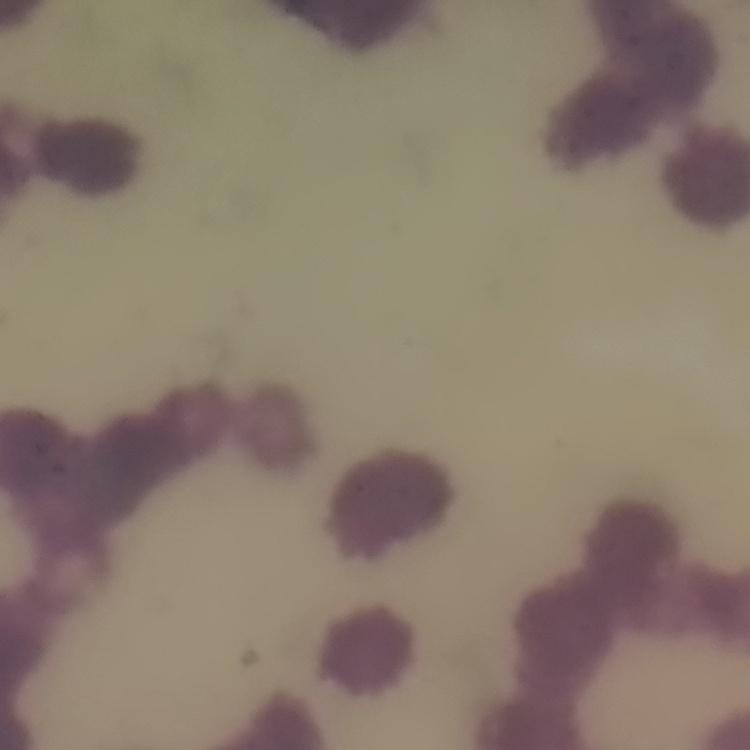 The red blood cells show rouleaux formation. Stained with either Field's or Giemsa. Thin blood film. Square crop of a larger photomicrograph.